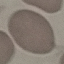

Malaria status: uninfected. Giemsa stain. Thin blood film. Acquired by smartphone through the microscope eyepiece. Cell patch, automatically extracted from a larger field of view and resized to 64 × 64 pixels.